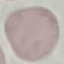
{
  "malaria_status": "uninfected",
  "capture": "smartphone camera at the microscope eyepiece",
  "stain": "Giemsa",
  "preparation": "thin blood smear",
  "image_type": "cell patch, automatically extracted from a larger field of view and resized to 64 × 64 pixels"
}